Comment on the morphology of the erythrocytes.
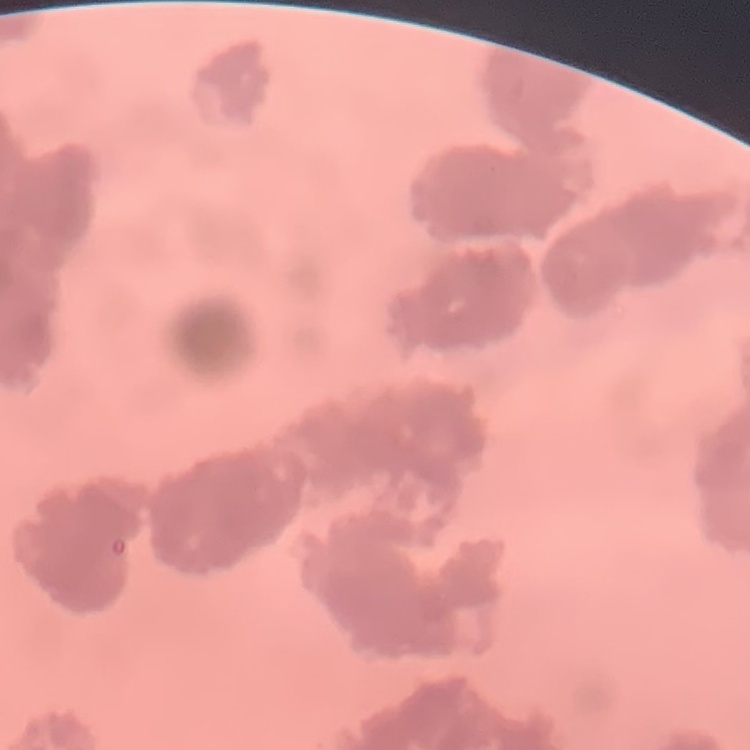

They show rouleaux formation.

image type = one tile cut from a larger photomicrograph
stain = Field's or Giemsa
preparation = thin blood smear